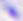
Summary:
  - Magnification: 400x
  - Modality: micrograph
  - Identification: Toxoplasma gondii